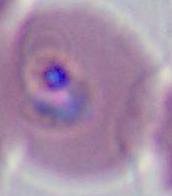
Photomicrograph. A Plasmodium parasite is shown. Captured at either 400x or 1000x magnification.